Identify the parasite.
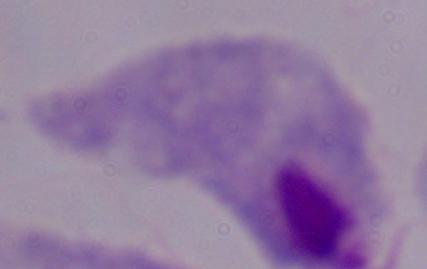

A trichomonad.

magnification: 1000x
modality: micrograph